Report the malaria status of this cell.
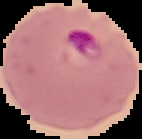
Parasitized.

Segmented cell region on a black background. From a thin blood film. Image is 142×139 pixels.